Name the cell type shown.
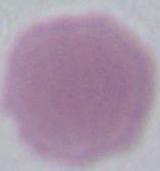
This is an erythrocyte.

magnification = 1000x
modality = micrograph